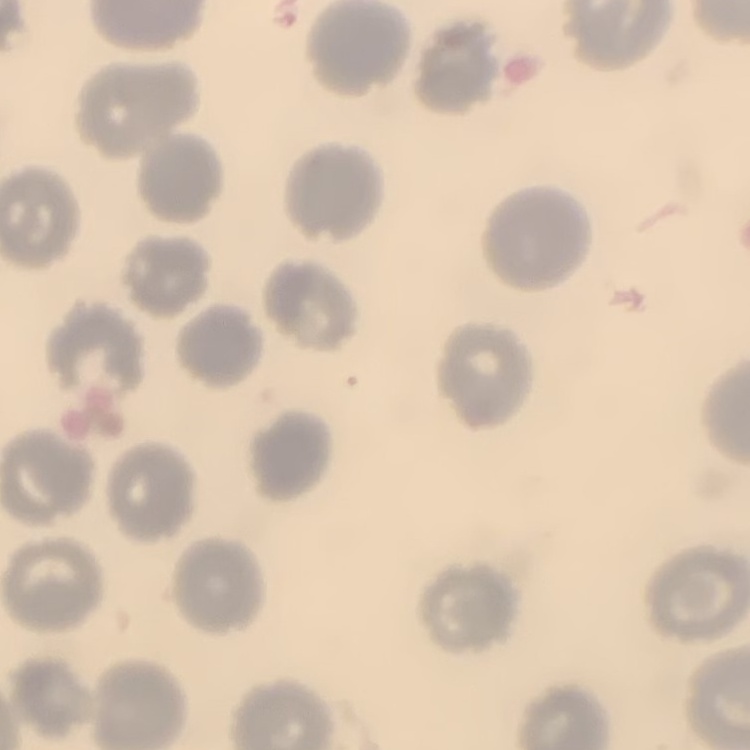 The erythrocytes show no rouleaux formation. Thin peripheral smear. One tile cut from a larger photomicrograph. Field's or Giemsa stain.